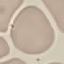

result = no malaria parasites seen
capture = smartphone camera at the microscope eyepiece
image type = cell patch, automatically extracted from a larger field of view and resized to 64 × 64 pixels
stain = Giemsa
preparation = thin blood smear